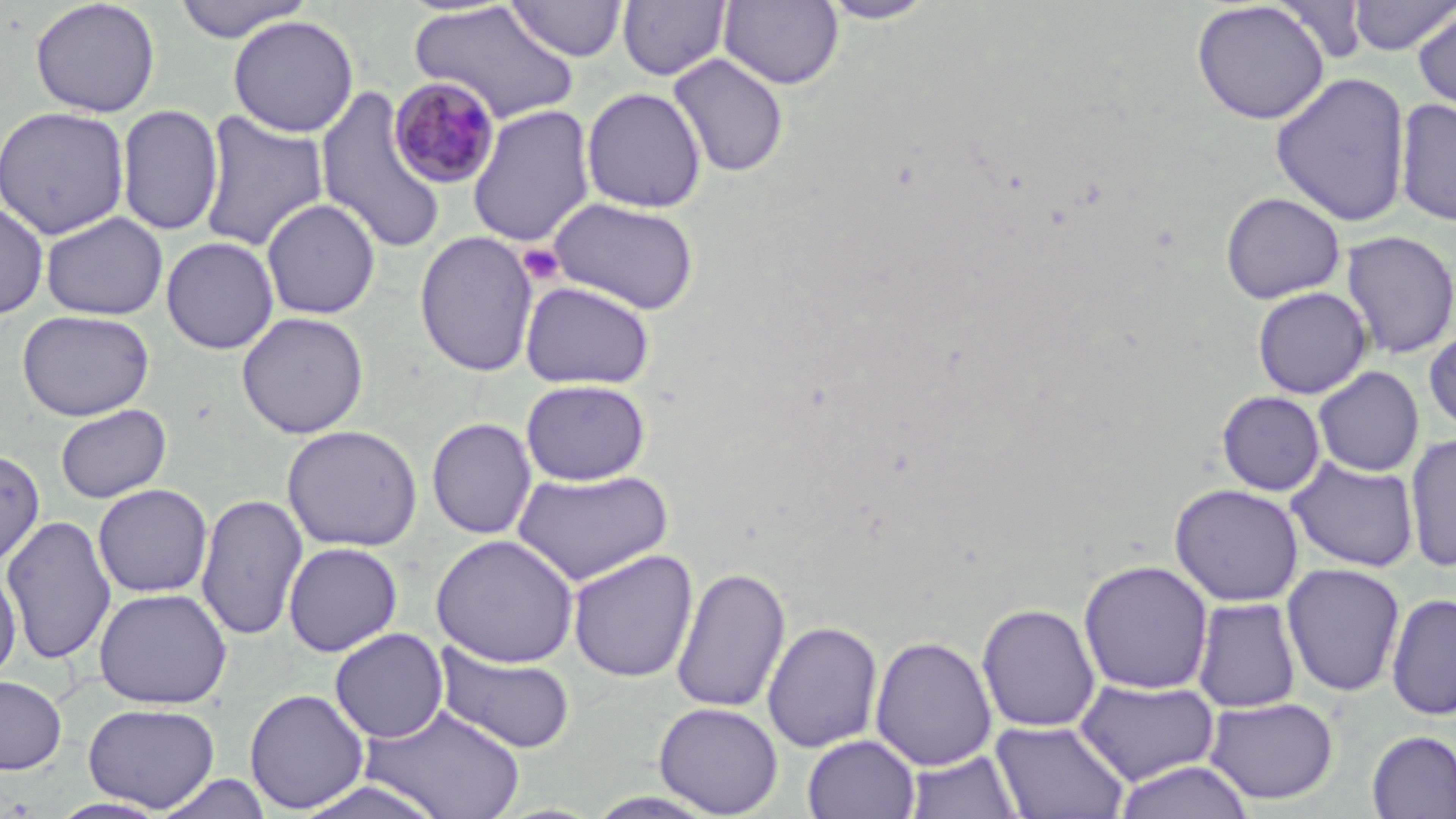

slide_level_diagnosis: Plasmodium malariae
field_of_view: single
uninfected_red_blood_cell_locations: 'approximate bounding boxes as (x1, y1, x2, y2) in pixels: (29, 0, 161, 118), (507, 0, 628, 61), (719, 0, 844, 90), (820, 0, 938, 24), (1190, 0, 1331, 125), (1348, 0, 1455, 60), (171, 1, 315, 42), (617, 1, 731, 81), (410, 3, 578, 124), (1412, 5, 1456, 118), (228, 14, 360, 138), (668, 53, 789, 178), (1270, 72, 1412, 227), (314, 86, 448, 254), (581, 87, 706, 213), (1395, 97, 1456, 227), (116, 104, 224, 237), (467, 104, 596, 248), (0, 105, 130, 240), (198, 110, 329, 253), (1219, 191, 1346, 304), (546, 197, 700, 315), (261, 198, 381, 319), (0, 201, 49, 320), (40, 211, 168, 321), (1340, 230, 1456, 360), (414, 231, 539, 377), (160, 236, 279, 354), (519, 280, 655, 390), (1252, 286, 1372, 399), (17, 309, 155, 421), (236, 311, 369, 439), (1423, 323, 1456, 436), (1313, 366, 1424, 477), (520, 378, 651, 486), (1216, 390, 1326, 496), (54, 404, 171, 503), (426, 416, 537, 539), (281, 424, 423, 552), (1404, 433, 1456, 573), (0, 448, 45, 568), (1286, 456, 1420, 573), (512, 468, 674, 587), (92, 483, 213, 598), (1169, 483, 1305, 607), (196, 492, 307, 641), (1, 514, 117, 666), (430, 533, 579, 667), (283, 541, 403, 657), (567, 549, 698, 683), (1078, 558, 1214, 695), (1281, 563, 1406, 697), (0, 564, 22, 683), (670, 566, 791, 714), (94, 587, 232, 709), (1385, 592, 1456, 722), (1192, 596, 1302, 714), (976, 602, 1101, 733), (761, 620, 883, 753), (329, 627, 449, 743), (869, 634, 997, 771), (433, 641, 577, 755), (0, 675, 67, 775), (1074, 677, 1220, 786), (244, 688, 370, 814), (1203, 696, 1339, 805), (653, 701, 783, 817), (82, 703, 220, 812), (362, 703, 525, 819), (990, 718, 1130, 819), (1366, 730, 1456, 819), (802, 734, 920, 819), (904, 749, 1024, 819), (1112, 760, 1256, 819), (154, 774, 274, 818), (293, 778, 451, 819), (47, 796, 172, 818)'
preparation: thin blood smear
magnification: 1000x
image_size: 1456×819 pixels
stain: May-Grünwald-Giemsa
platelet_locations: 'approximate bounding boxes as (x1, y1, x2, y2) in pixels: (518, 243, 565, 286)'
modality: optical microscopy
plasmodium_malariae_infected_red_blood_cell_locations: 'approximate bounding boxes as (x1, y1, x2, y2) in pixels: (388, 77, 502, 190)'